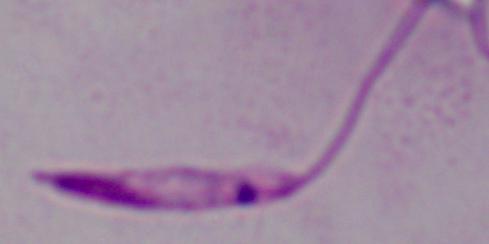

Summary:
  - Modality: photomicrograph
  - Magnification: 1000x
  - Identification: Leishmania